Locate and identify every blood parasite.
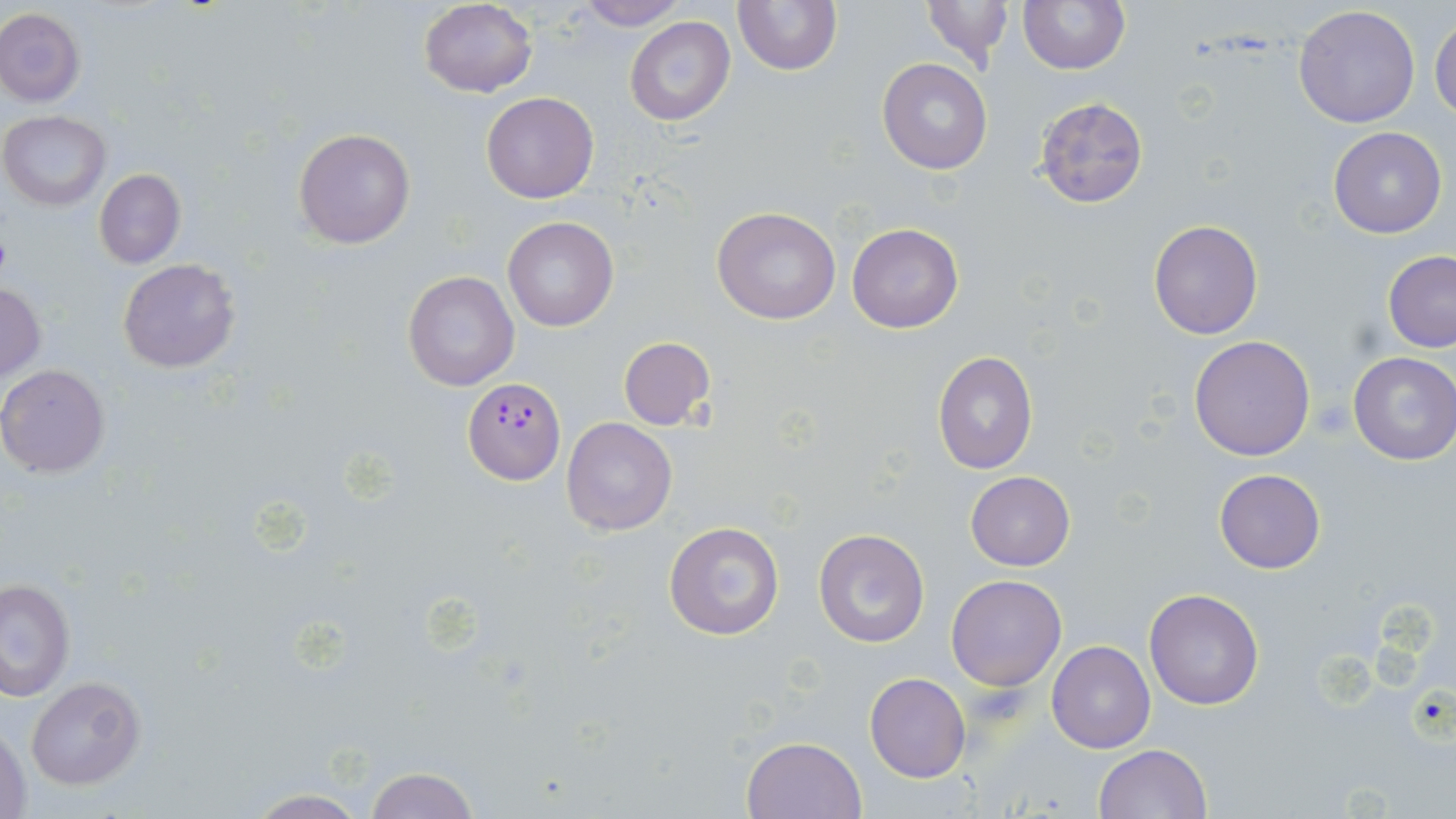
Approximate bounding boxes as (x1,y1)-(x2,y2) corner pairs in pixels.
Plasmodium falciparum-infected red blood cells: (462,381)-(567,485).
No Plasmodium ovale, Plasmodium malariae, Plasmodium vivax, Babesia divergens, or Trypanosoma brucei observed.

Summary:
  - Uninfected red blood cell locations: (571,0)-(686,29), (733,0)-(841,75), (920,0)-(1012,71), (1018,0)-(1129,74), (419,2)-(538,98), (1293,6)-(1421,129), (0,7)-(86,107), (624,16)-(735,126), (1430,17)-(1456,122), (878,58)-(992,174), (481,91)-(598,204), (1034,97)-(1150,206), (1,111)-(111,210), (294,127)-(416,249), (1329,127)-(1446,239), (94,169)-(185,268), (712,206)-(841,326), (503,216)-(618,331), (1148,219)-(1263,339), (847,223)-(964,333), (1381,251)-(1456,352), (117,257)-(239,373), (402,270)-(520,393), (0,282)-(46,381), (1188,335)-(1316,461), (619,336)-(717,430), (931,350)-(1038,474), (1348,352)-(1456,465), (0,363)-(113,479), (561,418)-(677,537), (1214,469)-(1327,575), (965,471)-(1074,571), (663,521)-(785,641), (813,528)-(930,647), (946,573)-(1067,691), (2,577)-(75,700), (1144,588)-(1263,711), (1046,640)-(1156,753), (865,672)-(971,783), (25,676)-(146,790), (1,723)-(30,819), (741,735)-(867,819), (1095,743)-(1212,819), (361,764)-(479,819), (242,790)-(373,819)
  - Slide-level diagnosis: Plasmodium falciparum
  - Preparation: thin blood smear
  - Modality: light microscopy
  - Field of view: one of a larger specimen
  - Stain: May-Grünwald-Giemsa
  - Magnification: 1000x
  - Image size: 1456×819 pixels